Report the malaria status of this cell.
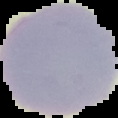

Uninfected.

From a thin blood smear. The area outside the segmented cell region is set to black. Image is 118×118 pixels.